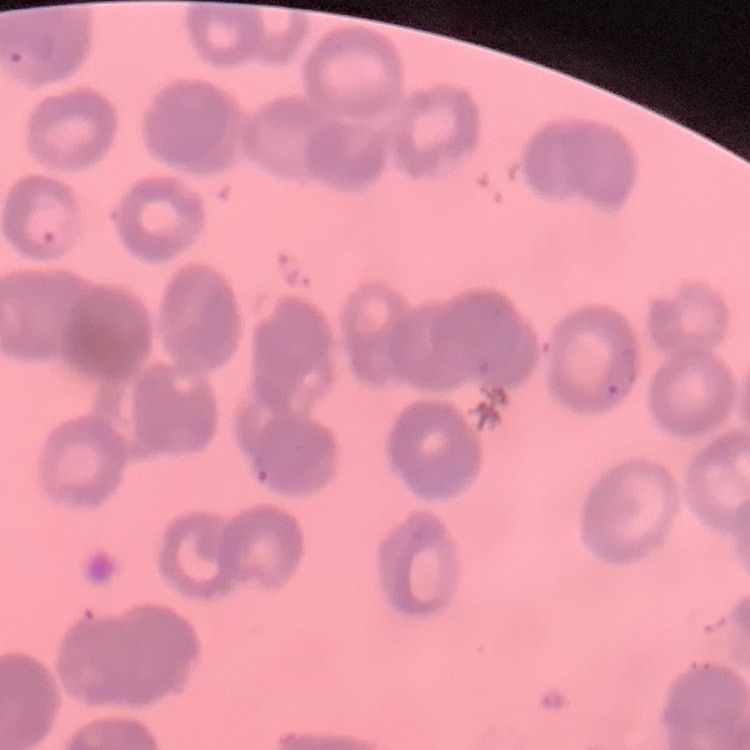

Summary:
  - Erythrocyte morphology: rouleaux formation
  - Image type: square crop of a larger photomicrograph
  - Preparation: thin peripheral smear
  - Stain: Field's or Giemsa